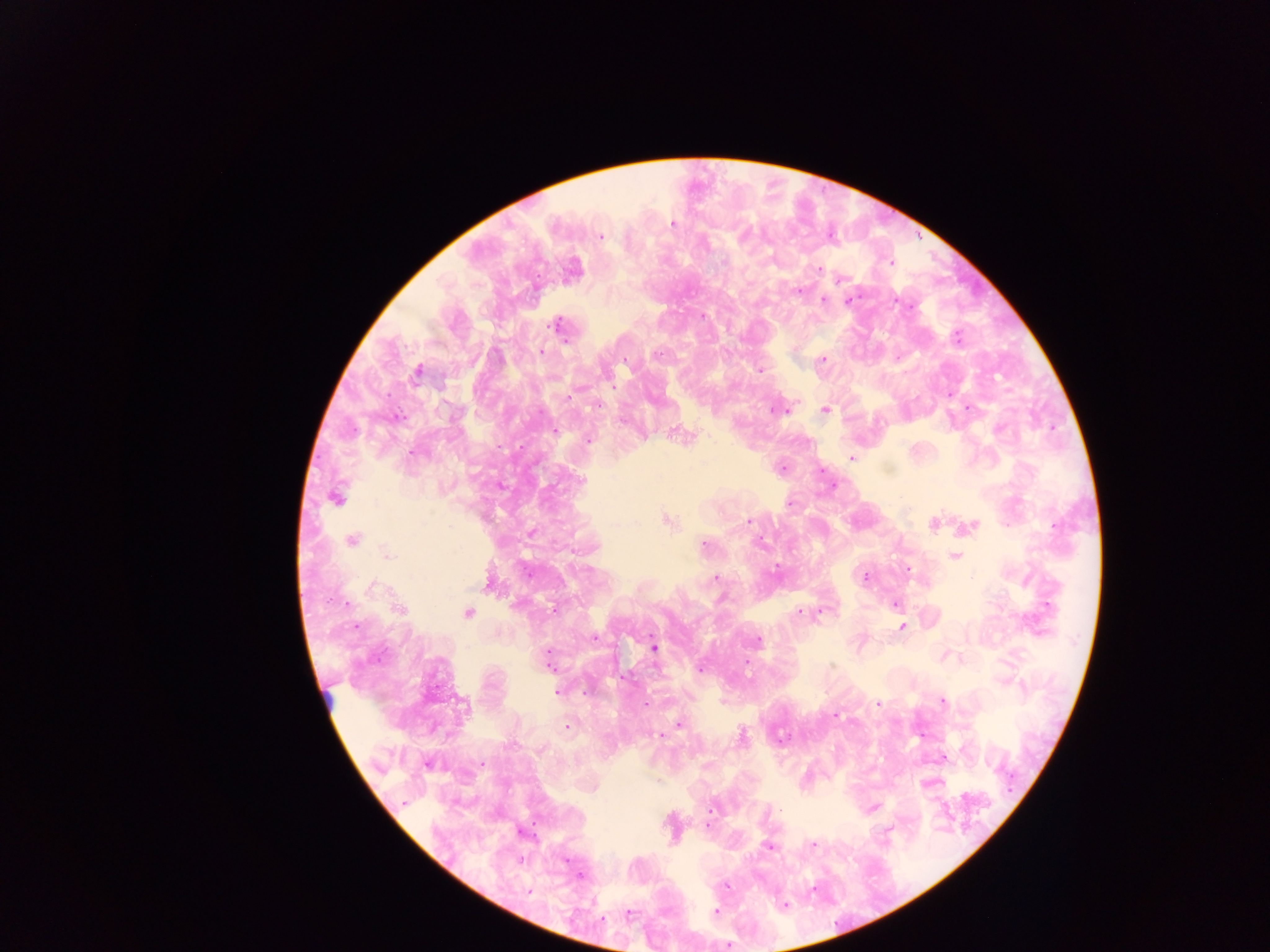

Approximate centers as x y in pixels. Plasmodium parasite locations: 672 224; 743 235; 601 237; 723 262; 890 262; 819 269; 840 279; 798 291; 824 300; 848 301; 555 325; 956 338; 497 353; 541 353; 656 355; 823 359; 626 360; 760 370; 417 371; 613 386; 569 397; 598 405; 967 408; 825 409; 774 410; 398 418; 555 430; 588 440; 413 453; 852 458; 782 468; 580 480; 336 497; 790 503; 669 522; 748 522; 934 524; 973 525; 352 540; 762 541; 704 546; 387 553; 955 557; 776 566; 908 569; 715 578; 865 578; 374 587; 345 604; 896 605; 1047 605; 554 609; 400 610; 822 611; 800 612; 468 613; 901 627; 595 637; 758 640; 654 647; 548 660; 701 669; 557 692; 942 700; 878 703; 644 704; 835 715; 679 723; 568 727; 742 735; 660 736; 428 764; 481 764; 594 789; 710 810; 708 825; 813 844; 768 847; 522 860; 580 875; 528 892; 783 905; 715 911; 629 913. Thick blood film. Collected in Ghana. Mobile-phone photograph taken through the microscope. One field of view. Image is 1270×952 pixels.